Report the malaria status of this cell.
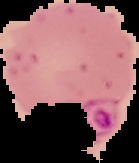
Parasitized.

{
  "image_size": "139×163 pixels",
  "preparation": "thin blood smear",
  "image_type": "segmented cell region on a black background"
}